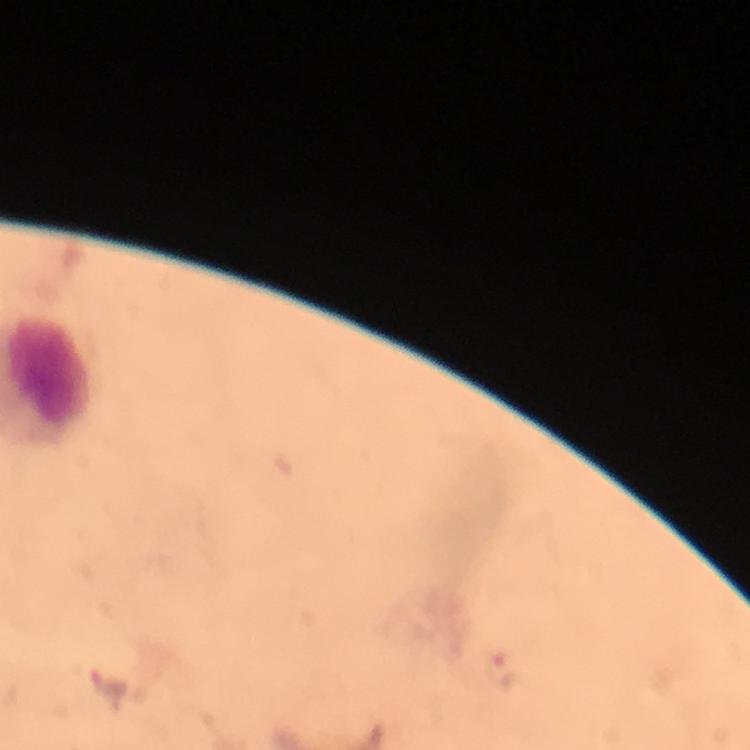
Approximate object centers, in pixels from the top-left corner.
Summary:
  - Plasmodium parasite locations: (x=503, y=672), (x=107, y=685)
  - Magnification: 100x
  - Preparation: thick smear
  - Stain: Giemsa
  - Cropped from: one field of view
  - Immersion oil: applied
  - Capture: smartphone camera through the microscope
  - Image size: 750×750 pixels
  - Context: from a diagnostic examination for malaria